Identify the preparation type.
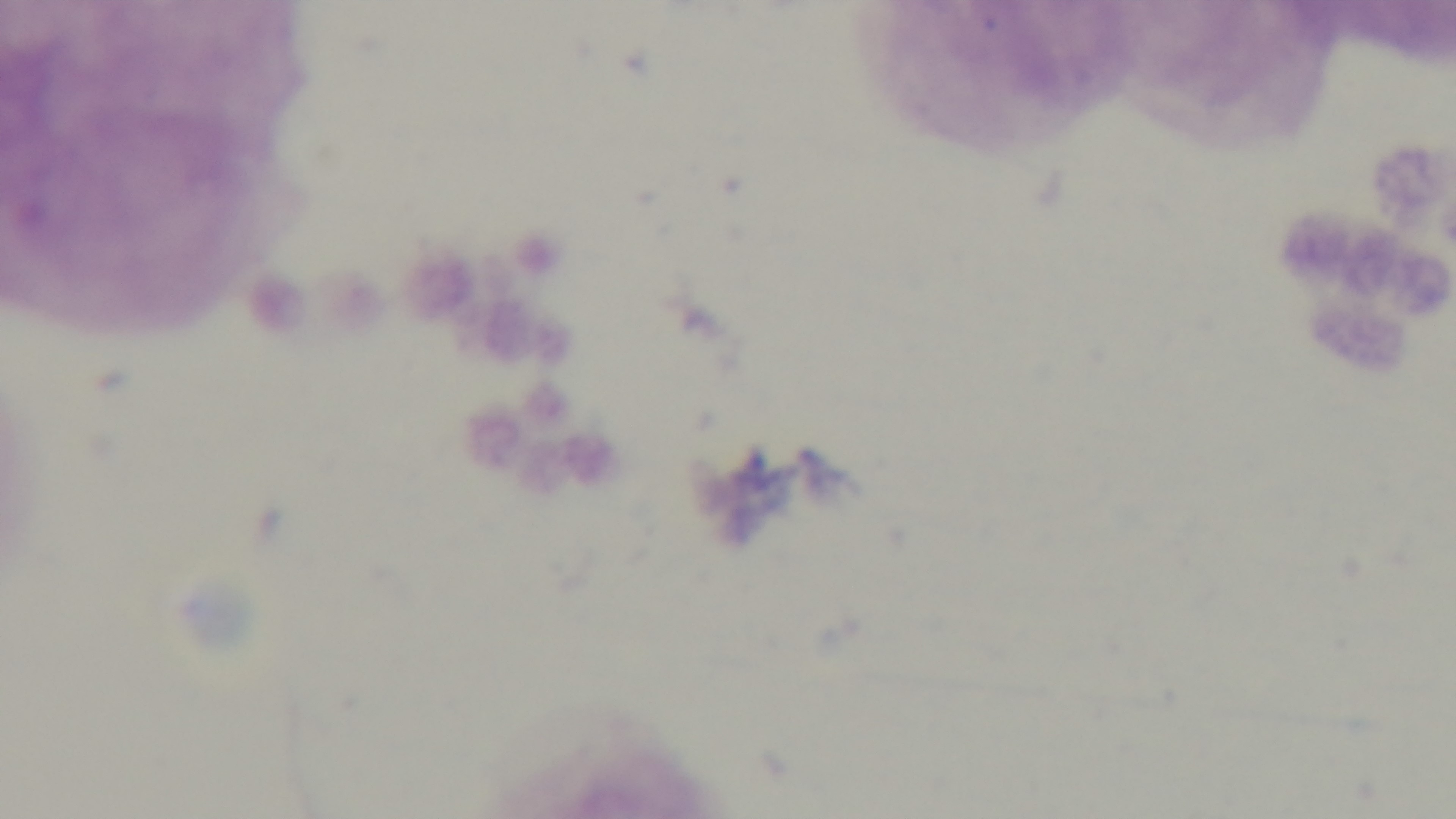
A thick smear.

field of view = one from the slide
capture = mounted 4K digital camera
objective = 100x oil immersion
stain = Giemsa
malaria status = uninfected
modality = light microscopy